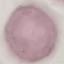

Summary:
  - Malaria status: uninfected
  - Image type: automatically extracted cell patch, resized to 64 × 64 pixels
  - Capture: smartphone camera at the microscope eyepiece
  - Stain: Giemsa
  - Preparation: thin smear